Draw a bounding box around every leukocyte (white blood cell).
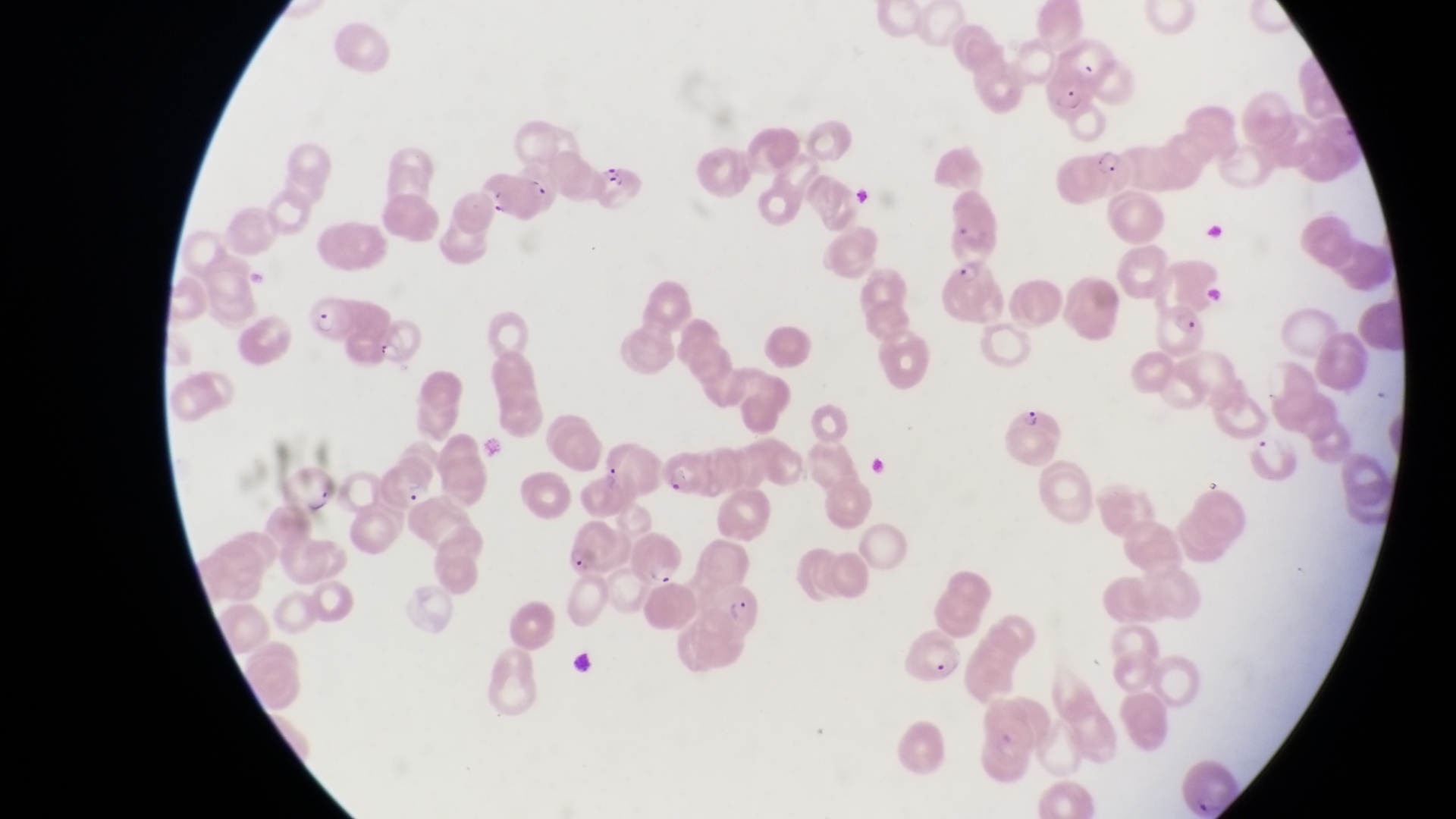

No leukocytes observed.

Approximate bounding boxes as [left, top, right, bottom] in pixels.
Summary:
  - Parasitised red blood cell locations: [1046, 79, 1098, 122], [1087, 142, 1136, 195], [595, 162, 641, 214], [482, 171, 545, 224], [940, 254, 1001, 321], [306, 296, 362, 343], [1158, 300, 1213, 359], [364, 315, 419, 365], [1004, 400, 1064, 466], [661, 449, 707, 496], [373, 457, 436, 507], [277, 462, 340, 518], [568, 516, 620, 577], [635, 531, 691, 586], [697, 571, 763, 634], [898, 631, 969, 691]
  - Magnification: 1000x
  - Country: Uganda
  - Capture: smartphone photograph through the eyepiece of an Olympus CX-23 microscope
  - Field of view: single
  - Preparation: thin blood film
  - Image size: 1456×819 pixels